State which parasite is depicted.
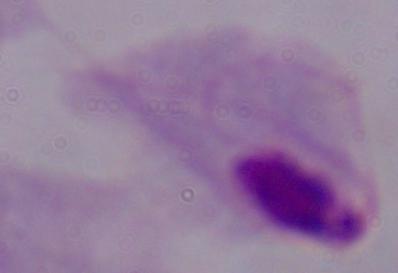

This is a trichomonad.

Summary:
  - Modality: photomicrograph
  - Magnification: 1000x